Locate every Plasmodium falciparum-infected red blood cell.
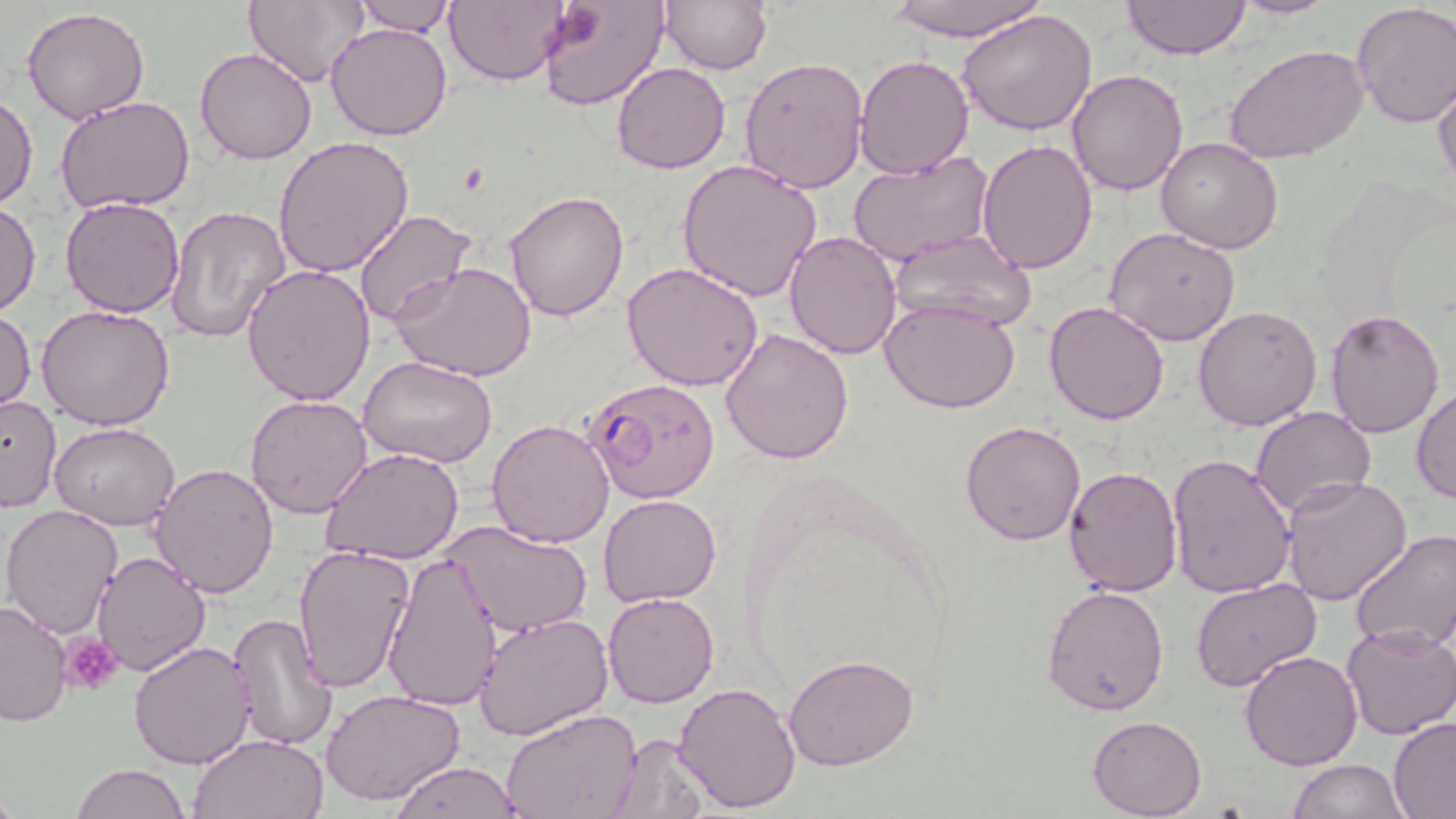

Approximate bounding boxes as [x1, y1, x2, y2] in pixels.
Plasmodium falciparum-infected red blood cells: [584, 375, 719, 503].

Platelet locations: [63, 633, 124, 695]. Uninfected red blood cell locations: [444, 0, 572, 86], [661, 0, 773, 74], [879, 0, 1050, 41], [1123, 0, 1251, 61], [1229, 0, 1338, 20], [353, 1, 458, 36], [538, 1, 671, 112], [244, 2, 367, 86], [1350, 2, 1456, 127], [22, 7, 150, 124], [957, 8, 1099, 138], [326, 23, 453, 141], [1225, 46, 1369, 165], [195, 47, 318, 165], [739, 55, 871, 194], [854, 55, 974, 180], [611, 61, 731, 174], [1065, 68, 1188, 196], [1433, 75, 1456, 191], [0, 91, 37, 210], [55, 96, 195, 215], [273, 136, 414, 277], [1157, 137, 1283, 255], [977, 139, 1097, 274], [847, 155, 993, 267], [676, 159, 823, 303], [504, 189, 631, 321], [61, 197, 184, 318], [0, 199, 40, 318], [165, 204, 291, 342], [354, 210, 477, 325], [1104, 228, 1242, 348], [784, 230, 903, 358], [889, 231, 1037, 332], [392, 261, 539, 384], [623, 263, 767, 392], [241, 264, 376, 406], [879, 297, 1020, 413], [1045, 301, 1168, 425], [35, 304, 176, 431], [1194, 304, 1323, 430], [0, 308, 36, 415], [1325, 308, 1445, 438], [721, 327, 855, 465], [357, 357, 500, 470], [1411, 386, 1456, 505], [245, 393, 373, 519], [0, 395, 62, 512], [1250, 406, 1376, 515], [486, 419, 616, 548], [959, 421, 1085, 545], [50, 422, 181, 531], [323, 446, 466, 566], [1165, 453, 1297, 600], [147, 461, 279, 598], [1063, 464, 1183, 598], [1280, 476, 1414, 607], [597, 494, 723, 607], [0, 502, 125, 638], [444, 519, 589, 637], [1350, 529, 1456, 653], [292, 543, 413, 692], [381, 550, 502, 714], [92, 551, 210, 678], [1191, 578, 1322, 693], [1042, 585, 1170, 716], [603, 593, 718, 708], [0, 601, 73, 726], [474, 611, 614, 742], [227, 613, 340, 754], [1341, 623, 1456, 741], [129, 642, 256, 770], [1240, 650, 1366, 771], [782, 652, 919, 771], [673, 681, 802, 814], [320, 688, 465, 807], [501, 709, 642, 819], [1087, 715, 1207, 818], [1388, 717, 1456, 818], [189, 731, 328, 819], [606, 732, 711, 818], [1288, 759, 1410, 818], [387, 760, 525, 818], [73, 763, 188, 819]. Slide-level diagnosis: Plasmodium falciparum. Optical microscopy. Captured at 1000x magnification. Single field of view. Image is 1456×819 pixels. Thin blood film. May-Grünwald-Giemsa-stained preparation.